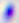 Toxoplasma gondii is shown. Captured at 400x magnification. Photomicrograph.